Name the parasite shown.
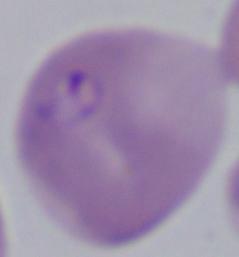
Babesia.

Photomicrograph. Captured at 1000x magnification.